Name the cell type shown.
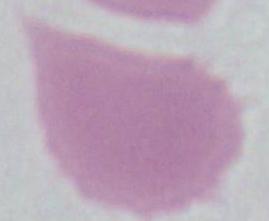
An erythrocyte.

{
  "magnification": "1000x",
  "modality": "micrograph"
}